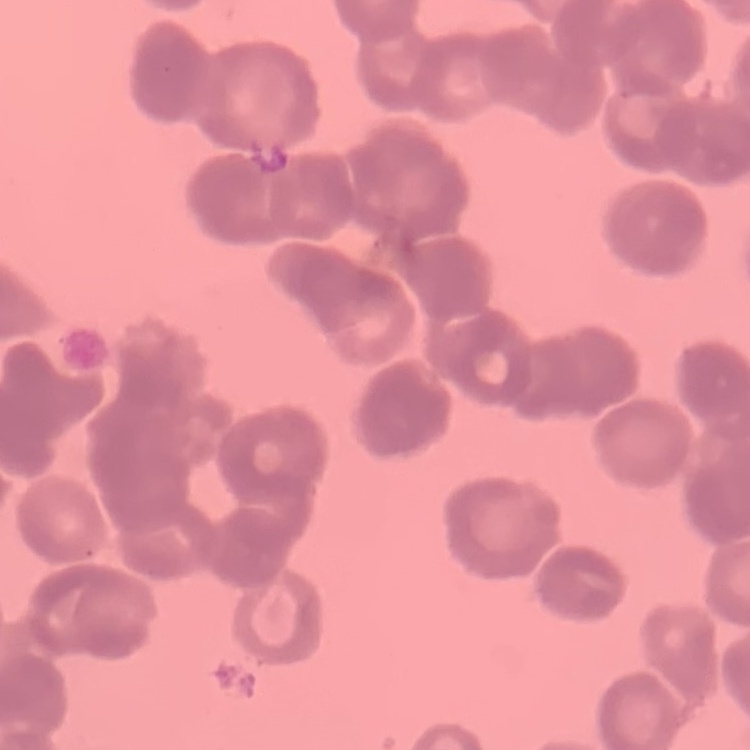

Summary:
  - Red blood cell morphology: rouleaux formation
  - Stain: Field's or Giemsa
  - Image type: square crop of a larger photomicrograph
  - Preparation: thin blood smear